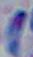
Toxoplasma gondii is shown. Micrograph. 1000x magnification.